Locate and identify every blood parasite.
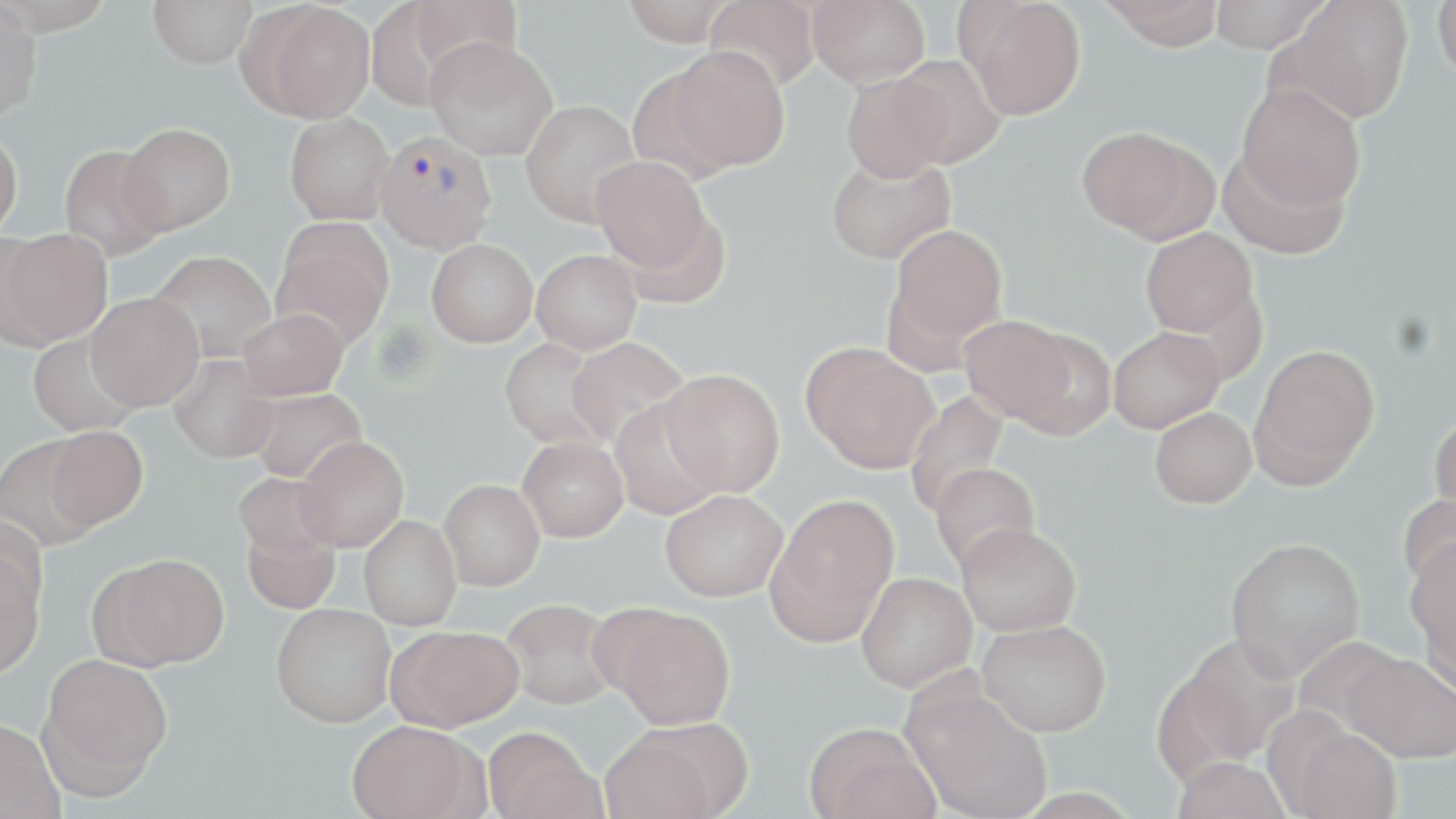

Approximate bounding boxes as named x1/y1/x2/y2 corners in pixels.
Plasmodium vivax-infected red blood cells: (x1=374, y1=130, x2=496, y2=254).
No Plasmodium falciparum, Plasmodium ovale, Plasmodium malariae, Babesia divergens, or Trypanosoma brucei observed.

Summary:
  - Uninfected red blood cell locations: (x1=148, y1=0, x2=257, y2=68), (x1=389, y1=0, x2=523, y2=93), (x1=621, y1=0, x2=736, y2=45), (x1=704, y1=0, x2=821, y2=92), (x1=807, y1=0, x2=931, y2=88), (x1=961, y1=0, x2=1086, y2=120), (x1=1099, y1=0, x2=1226, y2=50), (x1=1209, y1=0, x2=1331, y2=53), (x1=1280, y1=0, x2=1414, y2=124), (x1=1433, y1=0, x2=1456, y2=83), (x1=0, y1=1, x2=43, y2=120), (x1=251, y1=2, x2=375, y2=123), (x1=425, y1=37, x2=558, y2=160), (x1=667, y1=46, x2=790, y2=172), (x1=890, y1=54, x2=1007, y2=169), (x1=841, y1=71, x2=953, y2=182), (x1=1237, y1=84, x2=1366, y2=211), (x1=520, y1=99, x2=642, y2=227), (x1=285, y1=112, x2=395, y2=225), (x1=119, y1=123, x2=236, y2=234), (x1=1076, y1=126, x2=1205, y2=239), (x1=0, y1=127, x2=23, y2=241), (x1=58, y1=144, x2=168, y2=262), (x1=1217, y1=147, x2=1349, y2=260), (x1=825, y1=152, x2=956, y2=265), (x1=590, y1=156, x2=712, y2=273), (x1=622, y1=210, x2=731, y2=310), (x1=271, y1=221, x2=394, y2=348), (x1=887, y1=224, x2=1008, y2=353), (x1=2, y1=228, x2=112, y2=347), (x1=1140, y1=228, x2=1258, y2=339), (x1=426, y1=238, x2=538, y2=347), (x1=532, y1=249, x2=642, y2=354), (x1=149, y1=250, x2=276, y2=362), (x1=86, y1=293, x2=204, y2=410), (x1=237, y1=308, x2=348, y2=400), (x1=959, y1=316, x2=1076, y2=424), (x1=1107, y1=327, x2=1224, y2=433), (x1=1008, y1=328, x2=1116, y2=440), (x1=27, y1=331, x2=142, y2=437), (x1=566, y1=337, x2=690, y2=448), (x1=499, y1=338, x2=612, y2=450), (x1=801, y1=342, x2=938, y2=473), (x1=1250, y1=343, x2=1380, y2=485), (x1=169, y1=354, x2=280, y2=463), (x1=661, y1=368, x2=785, y2=496), (x1=247, y1=388, x2=367, y2=484), (x1=904, y1=390, x2=1009, y2=517), (x1=610, y1=399, x2=723, y2=521), (x1=1150, y1=407, x2=1257, y2=508), (x1=1429, y1=412, x2=1456, y2=522), (x1=46, y1=426, x2=148, y2=530), (x1=0, y1=436, x2=100, y2=552), (x1=295, y1=436, x2=409, y2=553), (x1=518, y1=437, x2=628, y2=542), (x1=928, y1=462, x2=1041, y2=574), (x1=233, y1=472, x2=341, y2=564), (x1=439, y1=479, x2=544, y2=591), (x1=660, y1=488, x2=788, y2=601), (x1=1398, y1=492, x2=1456, y2=594), (x1=766, y1=495, x2=899, y2=643), (x1=359, y1=514, x2=462, y2=630), (x1=241, y1=519, x2=341, y2=614), (x1=957, y1=522, x2=1082, y2=636), (x1=1225, y1=536, x2=1365, y2=680), (x1=1404, y1=537, x2=1456, y2=660), (x1=0, y1=541, x2=46, y2=679), (x1=90, y1=553, x2=228, y2=670), (x1=856, y1=572, x2=977, y2=692), (x1=1416, y1=590, x2=1456, y2=700), (x1=499, y1=598, x2=620, y2=710), (x1=271, y1=603, x2=396, y2=727), (x1=606, y1=606, x2=736, y2=729), (x1=977, y1=619, x2=1111, y2=736), (x1=391, y1=625, x2=525, y2=730), (x1=1178, y1=633, x2=1301, y2=763), (x1=37, y1=649, x2=173, y2=797), (x1=1344, y1=650, x2=1456, y2=763), (x1=905, y1=687, x2=1053, y2=819), (x1=0, y1=718, x2=63, y2=819), (x1=348, y1=719, x2=477, y2=819), (x1=805, y1=721, x2=937, y2=819), (x1=1281, y1=721, x2=1403, y2=819), (x1=484, y1=727, x2=602, y2=819), (x1=600, y1=727, x2=722, y2=819), (x1=1170, y1=756, x2=1292, y2=818)
  - Slide-level diagnosis: Plasmodium vivax
  - Field of view: one of a larger specimen
  - Stain: May-Grünwald-Giemsa
  - Magnification: 1000x
  - Modality: optical microscopy
  - Preparation: thin blood smear
  - Image size: 1456×819 pixels